Report the malaria status of this cell.
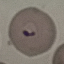
Parasitized.

Summary:
  - Stain: Giemsa
  - Preparation: thin smear
  - Image type: automatically extracted cell patch, resized to 64 × 64 pixels
  - Capture: smartphone through the microscope eyepiece